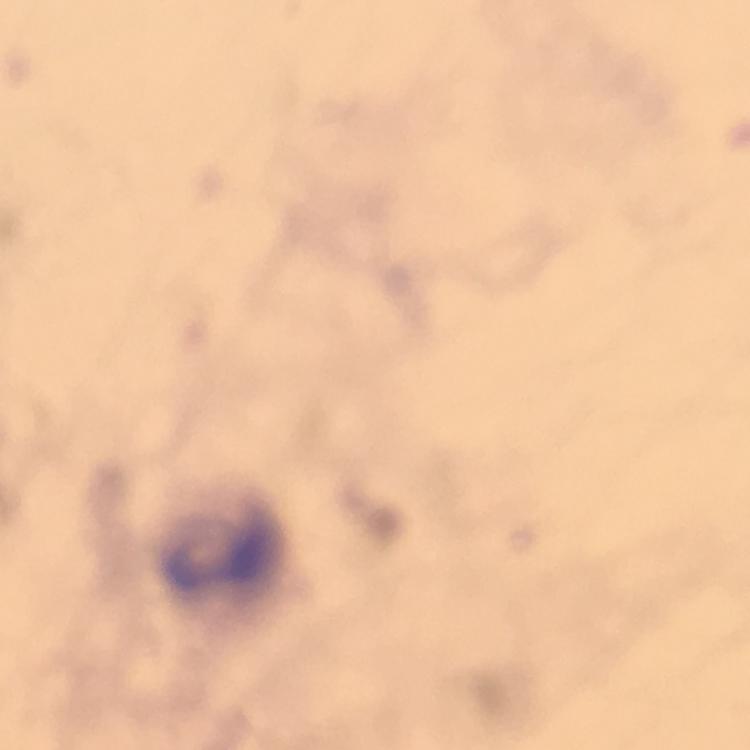

Approximate centers as (x, y) in pixels.
Summary:
  - Leukocyte locations: (220, 552)
  - Cropped from: one field of view
  - Magnification: 100x
  - Capture: smartphone mounted on the microscope
  - Stain: Giemsa
  - Plasmodium parasites: none detected
  - Context: from a malaria diagnostic workup
  - Image size: 750×750 pixels
  - Preparation: thick blood film
  - Immersion oil: applied